Report the malaria status of this cell.
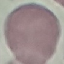

Uninfected.

Photographed with a smartphone camera at the microscope eyepiece. Thin blood film. Giemsa-stained preparation. Automatically extracted cell patch, resized to 64 × 64 pixels.